Outline platelets.
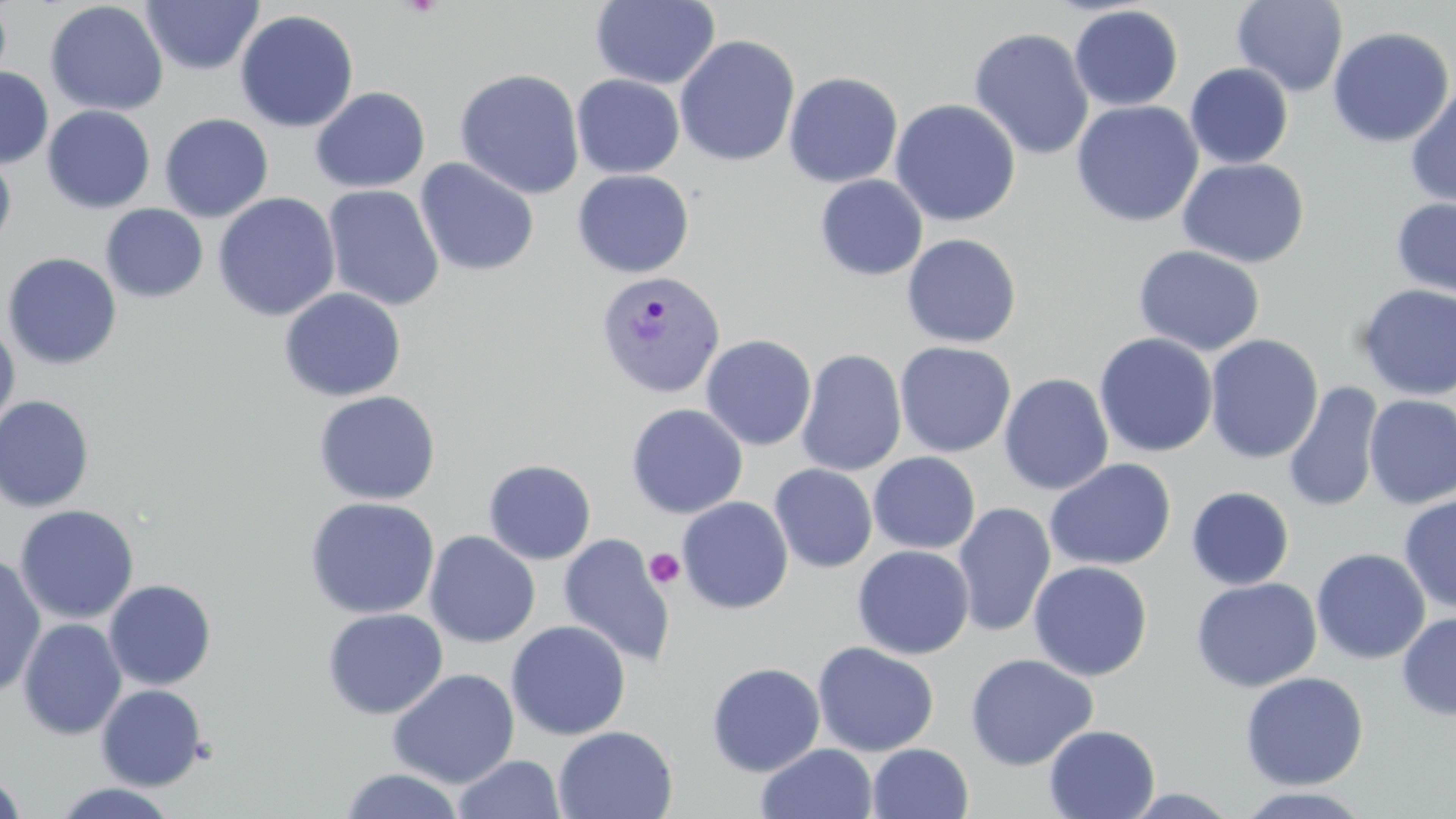
Approximate bounding boxes as (x1,y1)-(x2,y2) corner pairs in pixels.
Platelets: (644,548)-(686,589).

Uninfected red blood cell locations: (0,0)-(12,95), (590,0)-(721,89), (45,1)-(169,116), (141,1)-(263,75), (1232,1)-(1348,97), (1069,5)-(1183,112), (235,9)-(359,133), (1327,25)-(1455,149), (968,27)-(1094,161), (674,34)-(800,167), (1185,62)-(1294,169), (0,67)-(53,168), (454,68)-(585,199), (784,71)-(903,188), (571,74)-(684,178), (1404,84)-(1456,209), (310,86)-(431,193), (889,99)-(1021,227), (1070,100)-(1204,228), (42,105)-(155,213), (159,113)-(273,223), (0,148)-(17,252), (415,157)-(540,277), (1177,158)-(1310,268), (572,169)-(695,278), (815,174)-(928,281), (323,185)-(444,311), (212,192)-(340,322), (1390,196)-(1456,303), (101,204)-(208,302), (901,233)-(1022,347), (1133,244)-(1266,356), (2,252)-(122,370), (1355,284)-(1456,401), (278,287)-(407,401), (0,317)-(20,439), (1094,332)-(1218,458), (700,334)-(817,451), (1204,334)-(1324,464), (894,341)-(1016,458), (795,349)-(907,476), (998,373)-(1114,495), (1284,382)-(1383,513), (313,389)-(441,505), (0,394)-(95,513), (1363,394)-(1456,508), (626,403)-(748,519), (867,451)-(981,555), (1044,458)-(1176,571), (483,459)-(596,565), (769,464)-(877,573), (1186,486)-(1295,590), (1398,493)-(1456,614), (304,496)-(440,619), (677,496)-(793,614), (952,502)-(1056,638), (15,504)-(139,625), (424,531)-(541,648), (557,533)-(676,667), (852,544)-(975,660), (1311,548)-(1430,664), (0,555)-(46,699), (1028,560)-(1152,681), (1191,577)-(1322,692), (103,579)-(217,690), (322,607)-(448,719), (1396,612)-(1456,720), (17,617)-(127,740), (505,621)-(631,740), (812,641)-(939,757), (964,653)-(1099,771), (706,662)-(826,776), (387,668)-(520,789), (1240,671)-(1369,790), (96,684)-(208,790), (1044,724)-(1160,819), (552,725)-(678,818), (756,743)-(878,819), (867,743)-(973,819), (452,754)-(565,818), (339,768)-(466,819), (0,771)-(28,819), (52,781)-(181,818), (1228,786)-(1376,818). Plasmodium vivax-infected red blood cell locations: (595,269)-(727,399). Slide-level diagnosis: Plasmodium vivax. 1000x magnification. Single field of view. Optical microscopy. Image is 1456×819 pixels. Thin blood film. May-Grünwald-Giemsa stain.